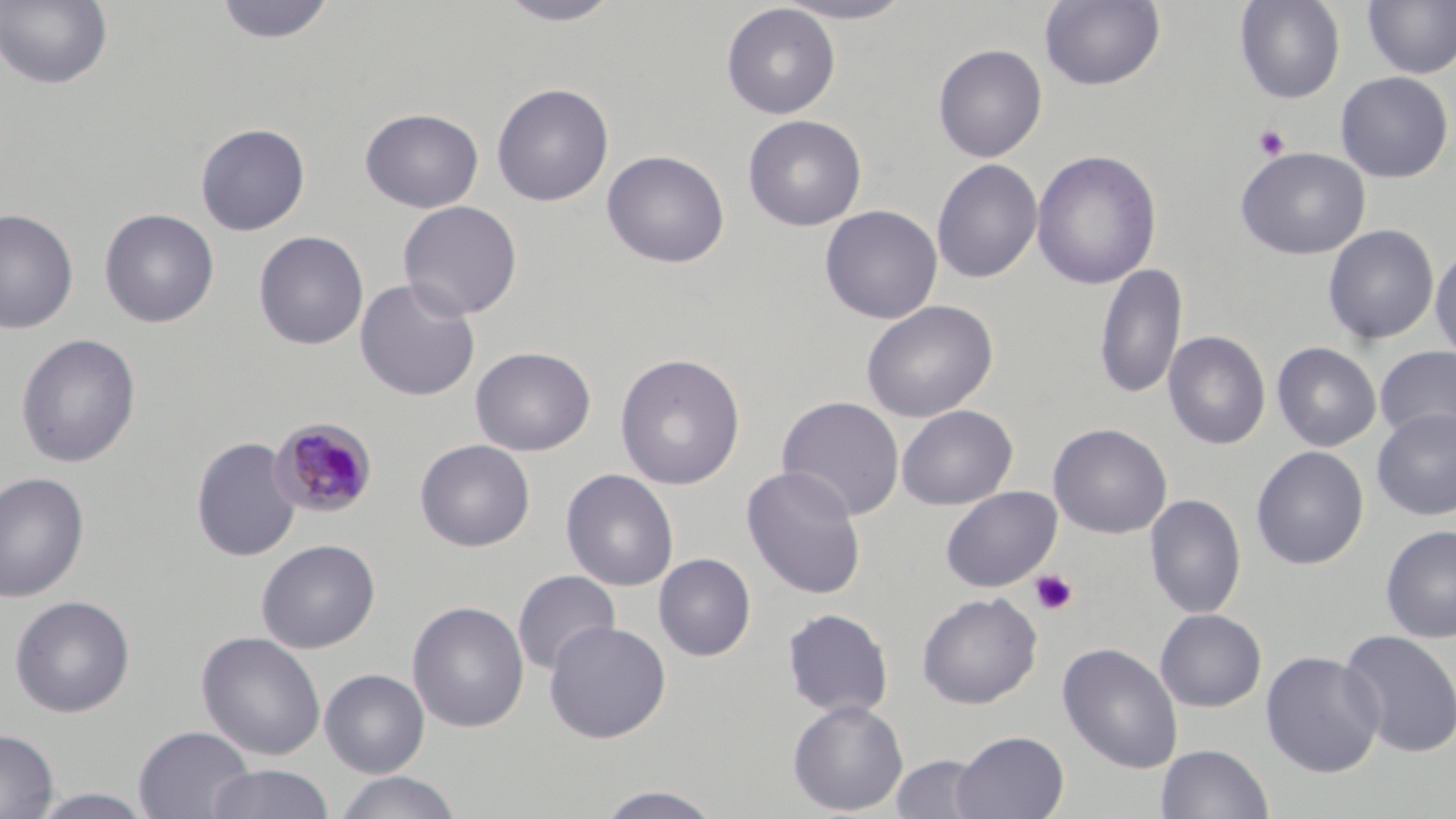

{
  "slide_level_diagnosis": "Plasmodium malariae",
  "field_of_view": "one of a larger specimen",
  "platelet_locations": "approximate bounding boxes as (x1, y1, x2, y2) in pixels: (1254, 124, 1290, 160), (1030, 569, 1078, 615)",
  "image_size": "1456×819 pixels",
  "preparation": "thin blood film",
  "plasmodium_malariae_infected_red_blood_cell_locations": "approximate bounding boxes as (x1, y1, x2, y2) in pixels: (269, 416, 378, 518)",
  "magnification": "1000x",
  "stain": "May-Grünwald-Giemsa",
  "modality": "optical microscopy",
  "uninfected_red_blood_cell_locations": "approximate bounding boxes as (x1, y1, x2, y2) in pixels: (215, 0, 335, 44), (494, 0, 627, 26), (770, 0, 918, 24), (1040, 0, 1165, 90), (1234, 0, 1345, 104), (0, 1, 113, 90), (1362, 1, 1456, 79), (721, 3, 841, 119), (933, 43, 1047, 163), (1335, 71, 1455, 183), (491, 82, 614, 206), (359, 107, 484, 212), (743, 114, 866, 231), (195, 123, 310, 235), (1236, 147, 1370, 260), (602, 149, 729, 268), (1031, 150, 1162, 290), (932, 158, 1043, 284), (398, 200, 523, 320), (820, 205, 943, 324), (0, 208, 78, 333), (99, 208, 219, 328), (1323, 224, 1438, 344), (253, 230, 369, 350), (1430, 243, 1456, 364), (1094, 262, 1188, 402), (354, 277, 480, 401), (860, 299, 999, 423), (1163, 330, 1270, 450), (15, 333, 141, 468), (1272, 342, 1381, 452), (1375, 345, 1456, 444), (470, 346, 596, 456), (614, 352, 746, 490), (777, 396, 905, 521), (896, 405, 1018, 510), (1371, 407, 1456, 521), (1048, 423, 1172, 538), (191, 437, 301, 562), (414, 439, 536, 552), (1251, 446, 1369, 570), (741, 465, 867, 600), (561, 468, 679, 592), (0, 471, 90, 603), (941, 486, 1061, 592), (1145, 493, 1246, 619), (1380, 524, 1456, 644), (256, 538, 380, 653), (653, 553, 756, 661), (512, 570, 621, 677), (917, 592, 1042, 708), (9, 595, 135, 717), (407, 600, 529, 733), (781, 608, 893, 719), (1155, 608, 1267, 711), (544, 620, 671, 743), (1339, 629, 1456, 759), (196, 631, 326, 761), (1058, 642, 1183, 773), (1261, 650, 1384, 778), (319, 668, 430, 778), (787, 699, 908, 815), (133, 725, 255, 819), (0, 728, 58, 819), (952, 730, 1069, 819), (1156, 743, 1274, 818), (889, 754, 989, 818), (205, 764, 335, 819), (332, 771, 463, 819), (590, 785, 727, 819), (27, 788, 156, 819)"
}